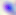
magnification: 400x
modality: micrograph
identification: Toxoplasma gondii